Point out leukocytes.
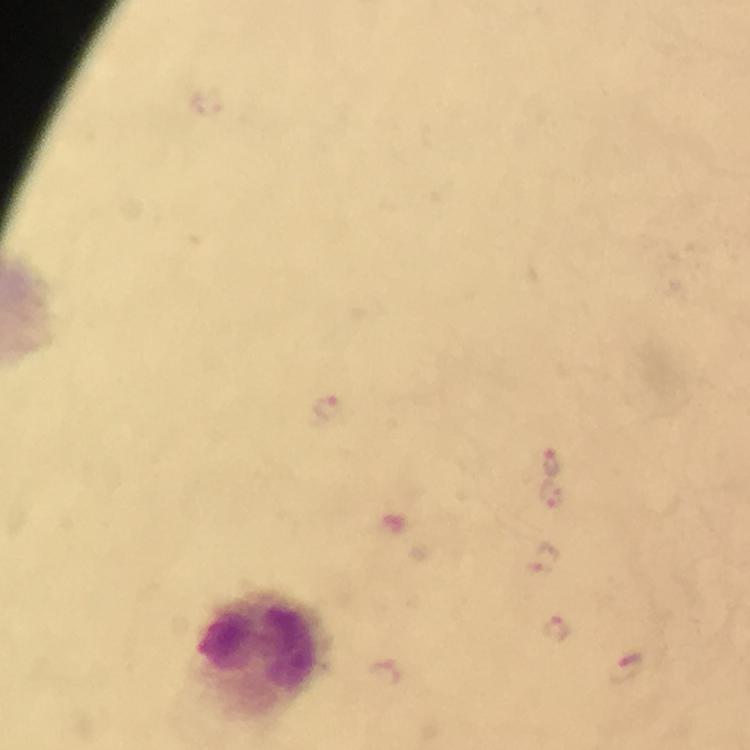

Approximate centers as {x, y} in pixels.
Leukocytes: {262, 653}.

Summary:
  - Plasmodium parasite locations: {330, 409}, {551, 460}, {551, 494}, {541, 560}, {556, 629}, {625, 668}, {383, 670}
  - Preparation: thick blood film
  - Image size: 750×750 pixels
  - Stain: Giemsa
  - Cropped from: one field of view
  - Immersion oil: used
  - Context: from a malaria diagnostic workup
  - Capture: smartphone camera through the microscope
  - Magnification: 100x